Outline each uninfected red blood cell.
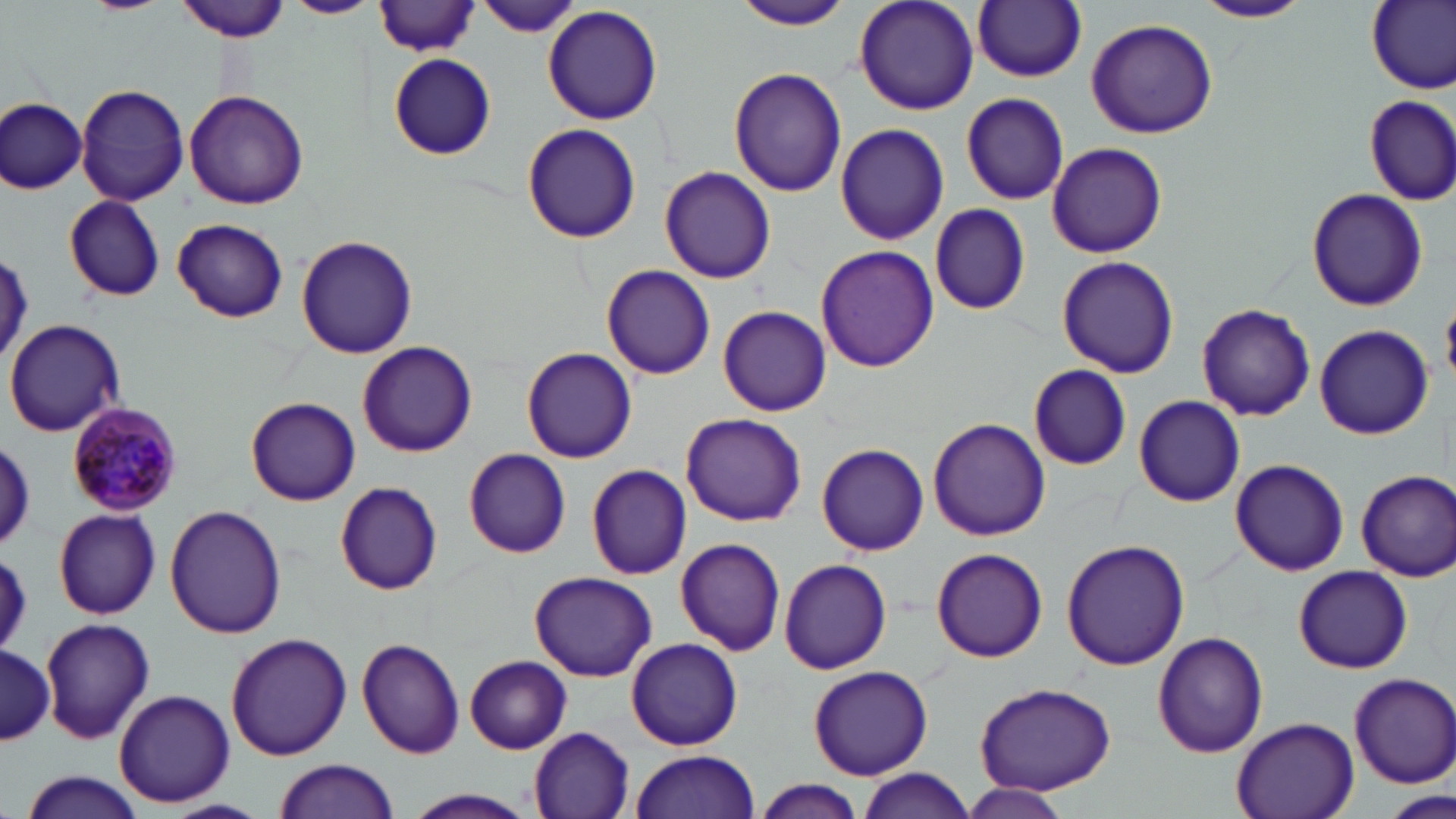

Approximate bounding boxes as [x1, y1, x2, y2] in pixels.
Uninfected red blood cells: [82, 0, 167, 15], [176, 0, 293, 42], [284, 0, 379, 19], [729, 0, 855, 30], [853, 0, 980, 116], [1194, 0, 1312, 23], [1364, 0, 1456, 93], [376, 1, 482, 56], [476, 1, 581, 39], [973, 1, 1087, 83], [543, 6, 663, 126], [1085, 18, 1219, 138], [388, 54, 497, 160], [729, 66, 847, 197], [76, 82, 190, 207], [186, 90, 309, 208], [960, 92, 1069, 205], [1364, 94, 1456, 205], [0, 98, 87, 193], [522, 122, 642, 244], [835, 123, 950, 247], [1046, 141, 1167, 256], [659, 166, 776, 284], [1306, 188, 1429, 312], [64, 197, 165, 302], [930, 203, 1031, 315], [172, 218, 289, 323], [296, 234, 418, 359], [815, 243, 940, 373], [1056, 253, 1179, 379], [601, 265, 716, 380], [1196, 303, 1317, 422], [718, 305, 831, 416], [5, 319, 126, 439], [1314, 325, 1432, 439], [357, 340, 478, 458], [521, 347, 637, 463], [1026, 364, 1132, 470], [1134, 395, 1244, 507], [245, 396, 361, 506], [681, 412, 806, 527], [927, 418, 1051, 541], [0, 438, 37, 549], [817, 443, 930, 556], [464, 448, 571, 558], [1230, 460, 1349, 576], [587, 464, 692, 580], [1356, 469, 1456, 581], [335, 482, 443, 595], [164, 505, 288, 637], [53, 507, 161, 620], [675, 537, 787, 656], [1062, 538, 1190, 670], [0, 547, 34, 654], [932, 547, 1048, 662], [779, 558, 890, 674], [1294, 564, 1412, 674], [528, 571, 658, 680], [41, 616, 154, 743], [1153, 630, 1267, 757], [225, 632, 352, 760], [355, 636, 465, 759], [625, 636, 743, 750], [0, 641, 56, 749], [463, 655, 572, 754], [809, 665, 933, 779], [1346, 671, 1456, 788], [974, 681, 1118, 795], [113, 690, 234, 805], [1232, 716, 1360, 819], [528, 725, 636, 818], [629, 750, 760, 819], [274, 757, 401, 818], [857, 768, 977, 819], [18, 770, 148, 819], [754, 778, 865, 819], [960, 783, 1070, 819], [1385, 787, 1449, 819], [402, 789, 538, 818].

Summary:
  - Plasmodium malariae-infected red blood cell locations: [65, 403, 181, 515]
  - Slide-level diagnosis: Plasmodium malariae
  - Magnification: 1000x
  - Field of view: one of a larger specimen
  - Modality: light microscopy
  - Image size: 1456×819 pixels
  - Stain: May-Grünwald-Giemsa
  - Preparation: thin blood film